Classify this cell by malaria status.
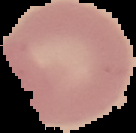
Uninfected.

Image is 136×133 pixels. From a thin blood film. Cell region segmented out of the field of view; the surrounding area is masked to black.